Classify this cell by malaria status.
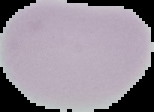
It is uninfected.

Image is 154×112 pixels. From a thin blood film. Cell region segmented out of the field of view; the surrounding area is masked to black.